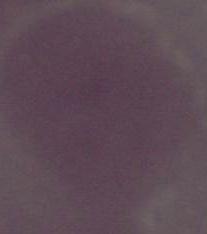
An erythrocyte is seen. Micrograph. Captured at 1000x magnification.